Give the extent of all Plasmodium falciparum-infected red blood cells.
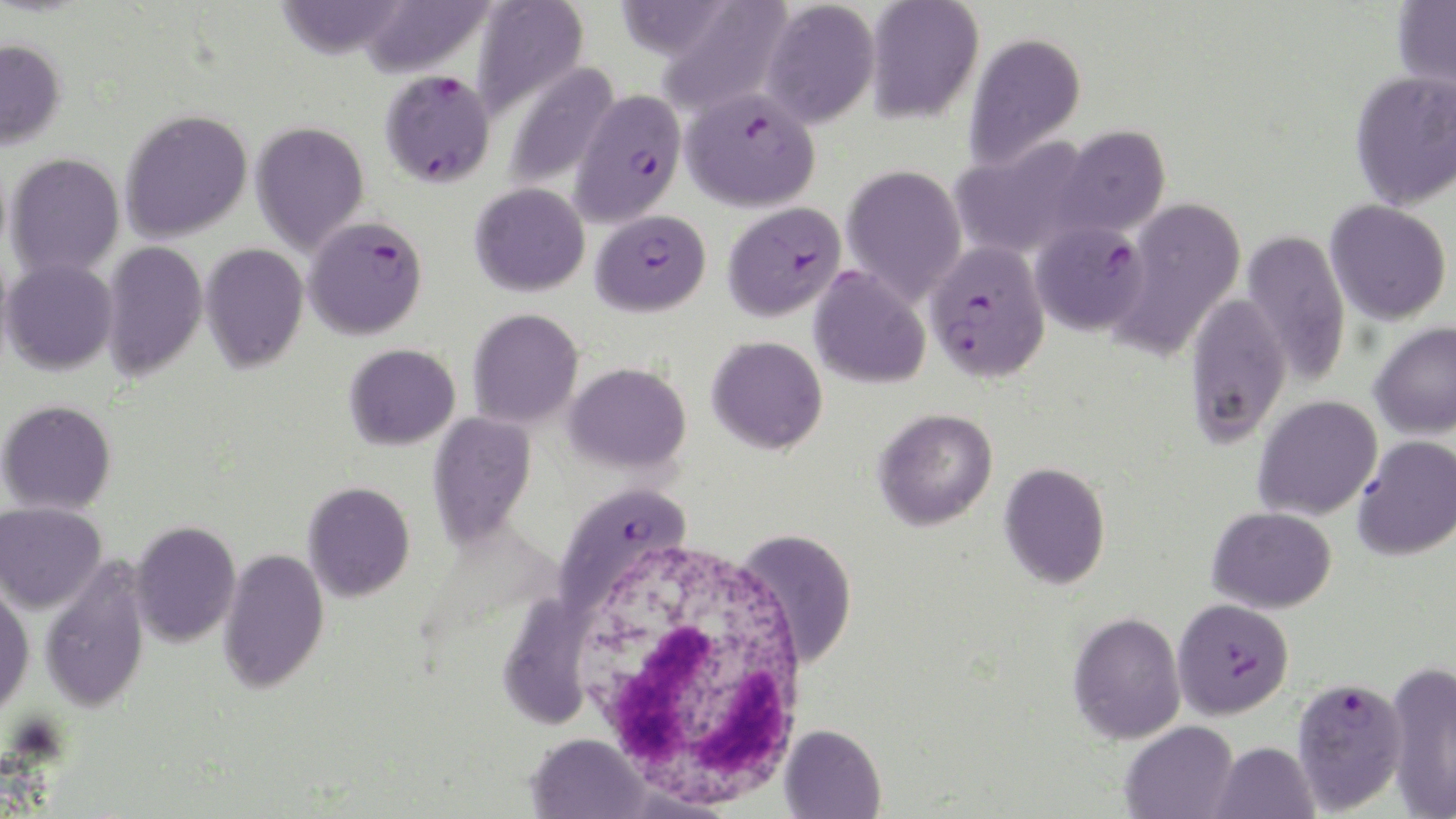
Approximate bounding boxes as [x1, y1, x2, y2] in pixels.
Plasmodium falciparum-infected red blood cells: [379, 70, 496, 189], [681, 85, 820, 212], [571, 90, 687, 225], [723, 201, 846, 321], [591, 209, 710, 316], [304, 215, 429, 340], [1030, 220, 1149, 336], [925, 240, 1050, 383], [556, 484, 692, 615], [1173, 598, 1294, 719], [1291, 675, 1408, 815].

Uninfected red blood cell locations: [274, 0, 410, 60], [358, 0, 494, 79], [472, 0, 589, 120], [760, 0, 880, 129], [864, 0, 984, 124], [1392, 0, 1456, 94], [610, 1, 736, 62], [655, 1, 794, 120], [963, 31, 1086, 170], [0, 38, 66, 150], [504, 61, 619, 191], [1349, 69, 1456, 210], [120, 109, 252, 243], [250, 121, 369, 257], [1050, 125, 1171, 239], [948, 137, 1096, 261], [6, 153, 125, 278], [841, 164, 967, 305], [470, 182, 589, 296], [1110, 197, 1246, 360], [1326, 200, 1452, 325], [1241, 229, 1351, 386], [101, 241, 207, 382], [199, 242, 308, 374], [1, 258, 118, 375], [808, 267, 931, 389], [1184, 292, 1291, 447], [468, 308, 583, 429], [1370, 321, 1456, 439], [706, 335, 828, 454], [344, 343, 460, 450], [565, 362, 691, 474], [1252, 395, 1382, 521], [1, 399, 116, 514], [873, 408, 997, 531], [427, 411, 537, 551], [1353, 435, 1456, 560], [998, 462, 1110, 589], [303, 481, 416, 602], [0, 501, 106, 614], [1206, 506, 1337, 613], [129, 520, 240, 648], [735, 529, 857, 667], [218, 548, 329, 694], [39, 559, 151, 714], [0, 586, 35, 716], [498, 593, 596, 730], [1067, 611, 1186, 744], [1385, 658, 1456, 818], [1120, 720, 1238, 819], [779, 723, 886, 819], [526, 732, 650, 819], [1208, 741, 1320, 819]. White blood cell locations: [575, 545, 811, 810]. Slide-level diagnosis: Plasmodium falciparum. May-Grünwald-Giemsa-stained preparation. Light microscopy. 1000x magnification. Image is 1456×819 pixels. One field of a larger specimen. Thin blood film.